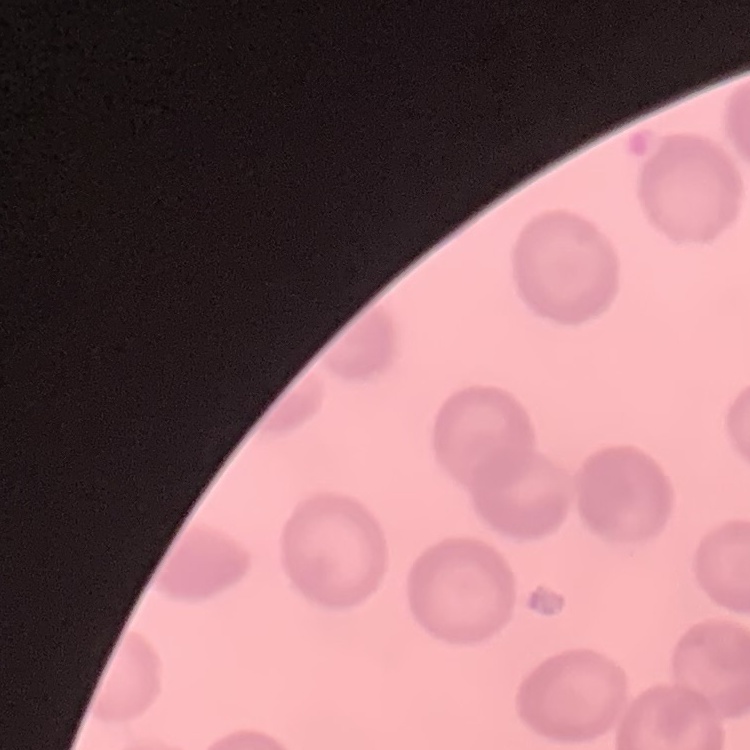

{
  "erythrocyte_morphology": "no rouleaux formation",
  "preparation": "thin peripheral smear",
  "stain": "Field's or Giemsa",
  "image_type": "square crop of a larger photomicrograph"
}